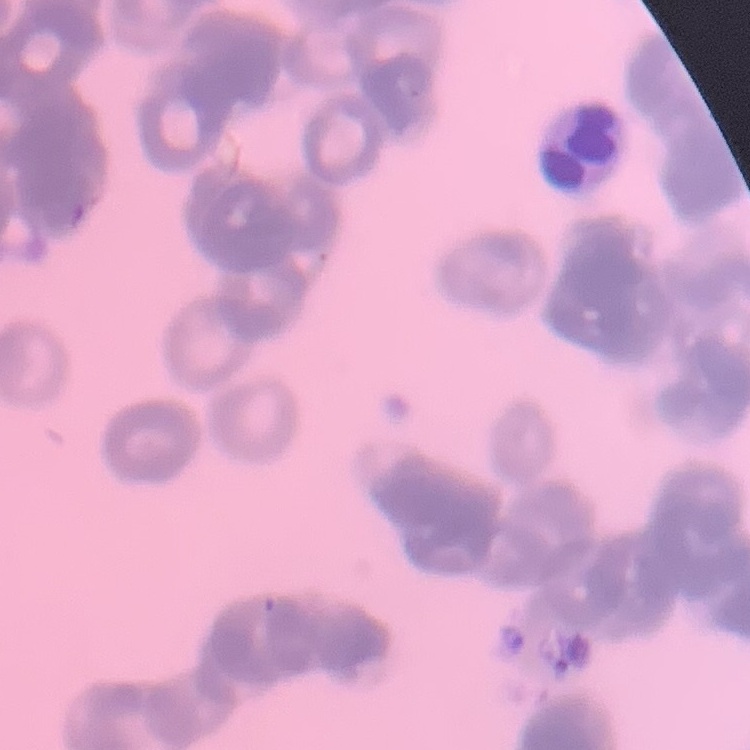

Summary:
  - Erythrocyte morphology: rouleaux formation
  - Image type: one tile cut from a larger photomicrograph
  - Stain: Field's or Giemsa
  - Preparation: thin peripheral smear